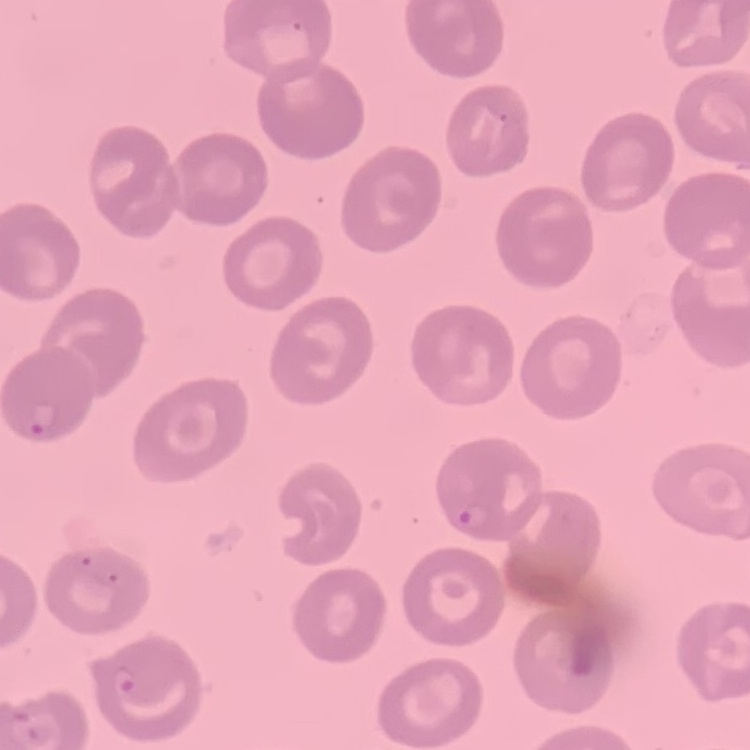

The red blood cells exhibit no rouleaux formation. Stained with either Field's or Giemsa. Thin blood film. One tile cut from a larger photomicrograph.